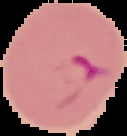

Malaria status: parasitized. From a thin blood film. Cell region segmented out of the field of view; the surrounding area is masked to black. Image is 127×136 pixels.